Describe the morphology of the red blood cells.
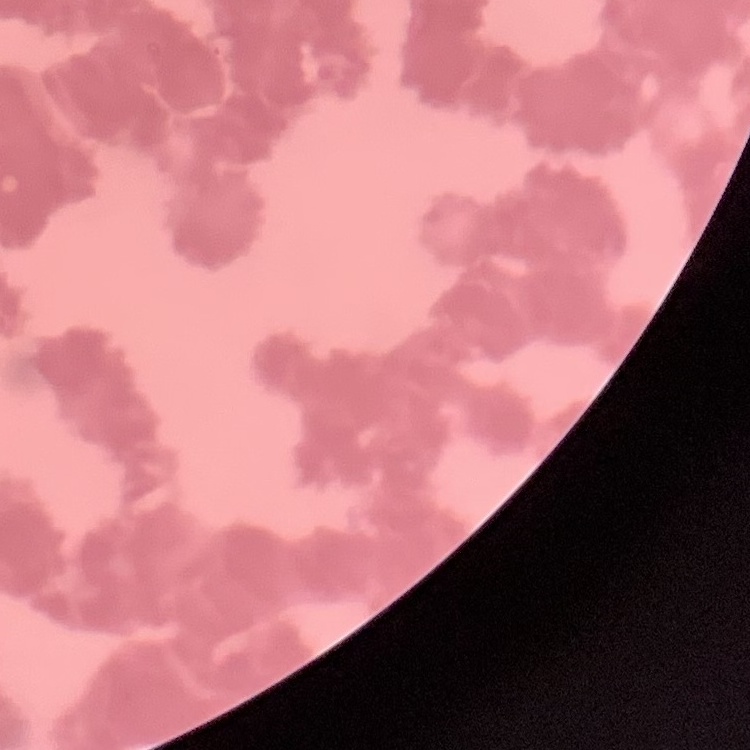
Rouleaux formation.

preparation = thin peripheral smear
stain = Field's or Giemsa
image type = square crop of a larger photomicrograph